Classify this cell by malaria status.
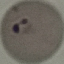
It is parasitized.

Cell patch, automatically extracted from a larger field of view and resized to 64 × 64 pixels. Photographed with a smartphone camera at the microscope eyepiece. Giemsa stain. Thin blood smear.